Locate every Plasmodium falciparum-infected red blood cell.
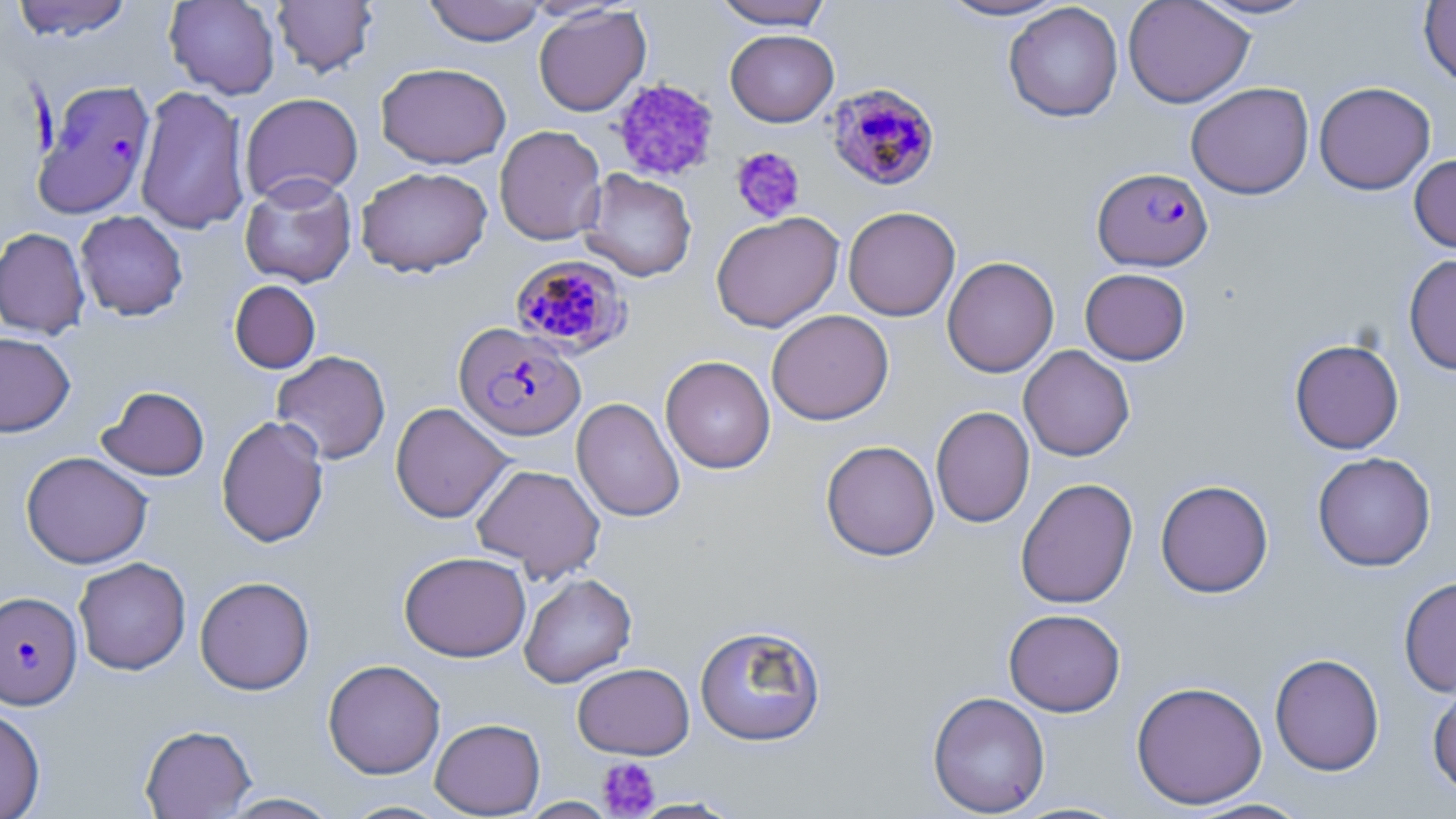

Approximate bounding boxes as (x1,y1)-(x2,y2) corner pairs in pixels.
Plasmodium falciparum-infected red blood cells: (28,76)-(153,216), (829,81)-(945,189), (1090,171)-(1211,274), (503,251)-(626,355), (454,323)-(586,441), (1,590)-(82,709).

Summary:
  - Platelet locations: (610,77)-(720,182), (730,147)-(805,224), (597,757)-(661,817)
  - Uninfected red blood cell locations: (11,0)-(133,41), (164,0)-(281,100), (272,0)-(378,77), (423,0)-(549,46), (712,0)-(833,29), (935,0)-(1071,21), (1122,0)-(1255,108), (1193,0)-(1321,21), (1418,1)-(1456,87), (1003,2)-(1123,122), (533,5)-(651,117), (725,29)-(839,127), (376,62)-(511,168), (1314,81)-(1436,194), (1186,82)-(1314,199), (134,85)-(250,235), (239,92)-(364,205), (494,125)-(607,245), (1409,154)-(1456,253), (356,166)-(492,277), (580,169)-(697,282), (239,174)-(357,288), (843,206)-(961,321), (75,210)-(188,321), (711,211)-(844,332), (0,227)-(90,339), (1404,253)-(1456,375), (941,256)-(1059,378), (1080,268)-(1191,365), (229,280)-(321,373), (767,309)-(894,425), (0,332)-(75,437), (1289,338)-(1404,454), (1018,344)-(1135,461), (272,350)-(391,464), (660,355)-(775,474), (97,386)-(210,481), (571,397)-(685,522), (390,402)-(513,523), (931,405)-(1035,528), (216,415)-(329,548), (820,440)-(939,561), (21,451)-(153,569), (1312,451)-(1436,571), (471,464)-(606,581), (1015,477)-(1139,609), (1155,480)-(1274,598), (399,551)-(531,661), (73,557)-(191,675), (519,573)-(637,688), (194,575)-(315,695), (1398,576)-(1456,698), (1003,608)-(1125,717), (694,624)-(826,746), (1269,653)-(1385,775), (322,659)-(446,779), (572,662)-(695,759), (1130,680)-(1268,809), (1427,682)-(1456,798), (927,691)-(1051,817), (0,705)-(46,819), (430,718)-(545,817), (139,724)-(256,818), (217,792)-(342,818), (520,797)-(617,818), (629,797)-(742,818), (1183,797)-(1317,818), (339,799)-(454,818)
  - Slide-level diagnosis: Plasmodium falciparum
  - Image size: 1456×819 pixels
  - Preparation: thin blood smear
  - Magnification: 1000x
  - Stain: May-Grünwald-Giemsa
  - Modality: optical microscopy
  - Field of view: single